Identify the blood parasite species.
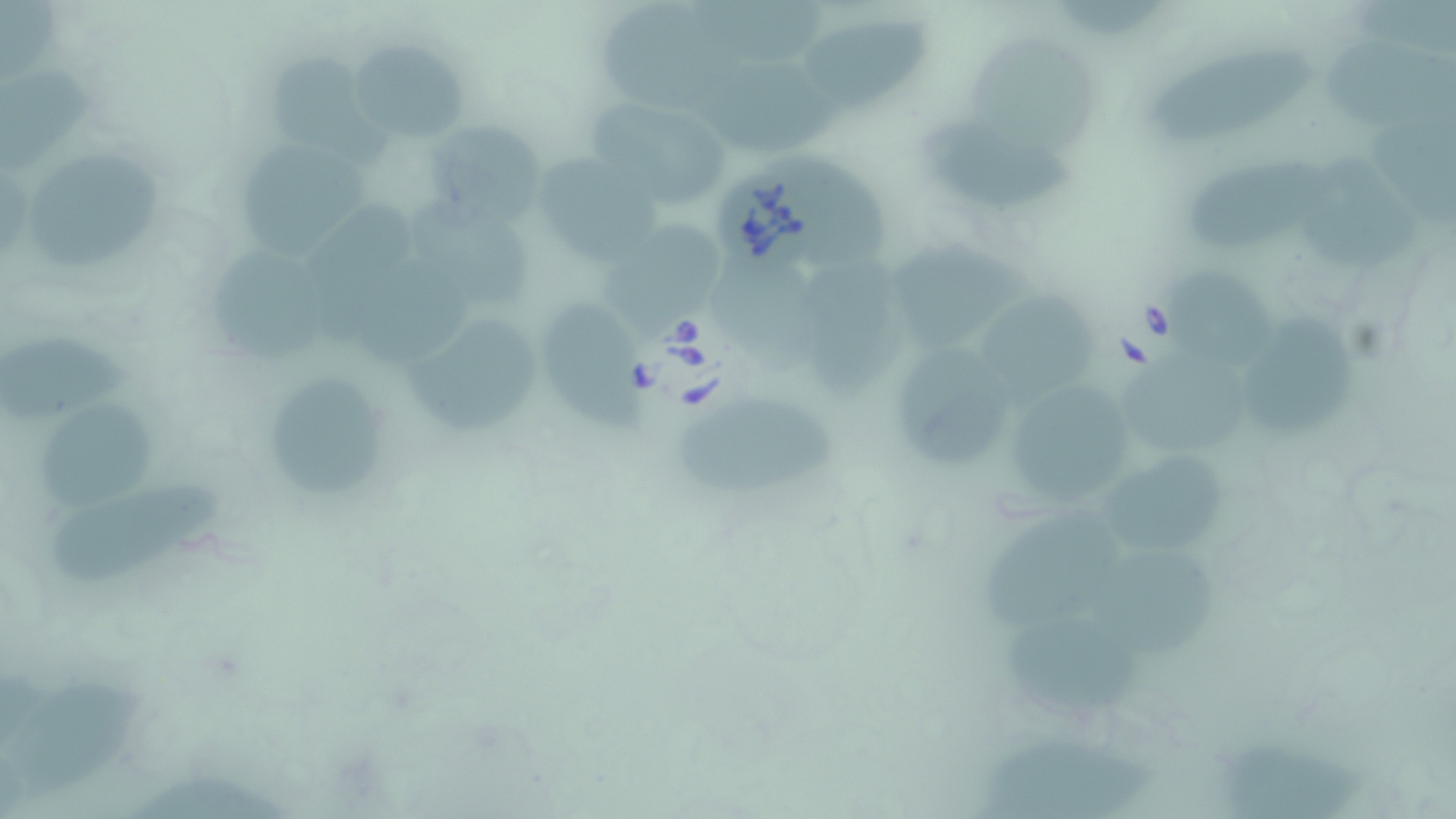
Babesia divergens.

Approximate bounding boxes as named x1/y1/x2/y2 corners in pixels. Babesia divergens-infected red blood cell locations: (x1=706, y1=166, x2=832, y2=275). Uninfected red blood cell locations: (x1=593, y1=4, x2=736, y2=117), (x1=800, y1=19, x2=933, y2=111), (x1=967, y1=33, x2=1098, y2=160), (x1=351, y1=34, x2=473, y2=149), (x1=1147, y1=49, x2=1317, y2=152), (x1=696, y1=59, x2=850, y2=152), (x1=3, y1=70, x2=93, y2=171), (x1=597, y1=101, x2=727, y2=208), (x1=918, y1=118, x2=1078, y2=209), (x1=435, y1=124, x2=545, y2=230), (x1=244, y1=140, x2=370, y2=257), (x1=542, y1=152, x2=661, y2=270), (x1=1308, y1=157, x2=1424, y2=277), (x1=33, y1=159, x2=161, y2=265), (x1=1192, y1=159, x2=1331, y2=249), (x1=413, y1=199, x2=535, y2=309), (x1=607, y1=220, x2=725, y2=334), (x1=209, y1=236, x2=330, y2=363), (x1=893, y1=238, x2=1038, y2=352), (x1=361, y1=257, x2=473, y2=369), (x1=813, y1=263, x2=906, y2=398), (x1=1166, y1=264, x2=1275, y2=375), (x1=713, y1=266, x2=834, y2=372), (x1=981, y1=283, x2=1097, y2=409), (x1=534, y1=299, x2=647, y2=433), (x1=1242, y1=318, x2=1355, y2=442), (x1=406, y1=321, x2=545, y2=435), (x1=2, y1=337, x2=136, y2=424), (x1=893, y1=342, x2=1010, y2=470), (x1=1123, y1=357, x2=1258, y2=455), (x1=269, y1=378, x2=391, y2=497), (x1=1008, y1=383, x2=1134, y2=505), (x1=677, y1=402, x2=837, y2=497), (x1=37, y1=406, x2=155, y2=514), (x1=1100, y1=445, x2=1231, y2=558), (x1=52, y1=481, x2=227, y2=580), (x1=982, y1=510, x2=1122, y2=629), (x1=1098, y1=547, x2=1223, y2=659), (x1=1006, y1=605, x2=1141, y2=714), (x1=4, y1=678, x2=147, y2=791), (x1=1219, y1=732, x2=1362, y2=819), (x1=979, y1=742, x2=1162, y2=819). Light microscopy. Single field of view. May-Grünwald-Giemsa-stained preparation. Image is 1456×819 pixels. Thin blood smear. 1000x magnification.